Report the malaria status of this cell.
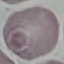
It is uninfected.

Summary:
  - Capture: smartphone camera at the microscope eyepiece
  - Preparation: thin blood film
  - Image type: cell patch, automatically extracted from a larger field of view and resized to 64 × 64 pixels
  - Stain: Giemsa